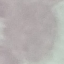
Summary:
  - Malaria status: uninfected
  - Image type: automatically extracted cell patch, resized to 64 × 64 pixels
  - Stain: Giemsa
  - Capture: smartphone through the microscope eyepiece
  - Preparation: thin blood film